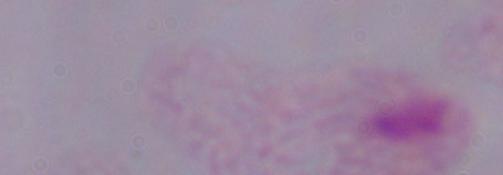
identification = trichomonad
magnification = 1000x
modality = photomicrograph